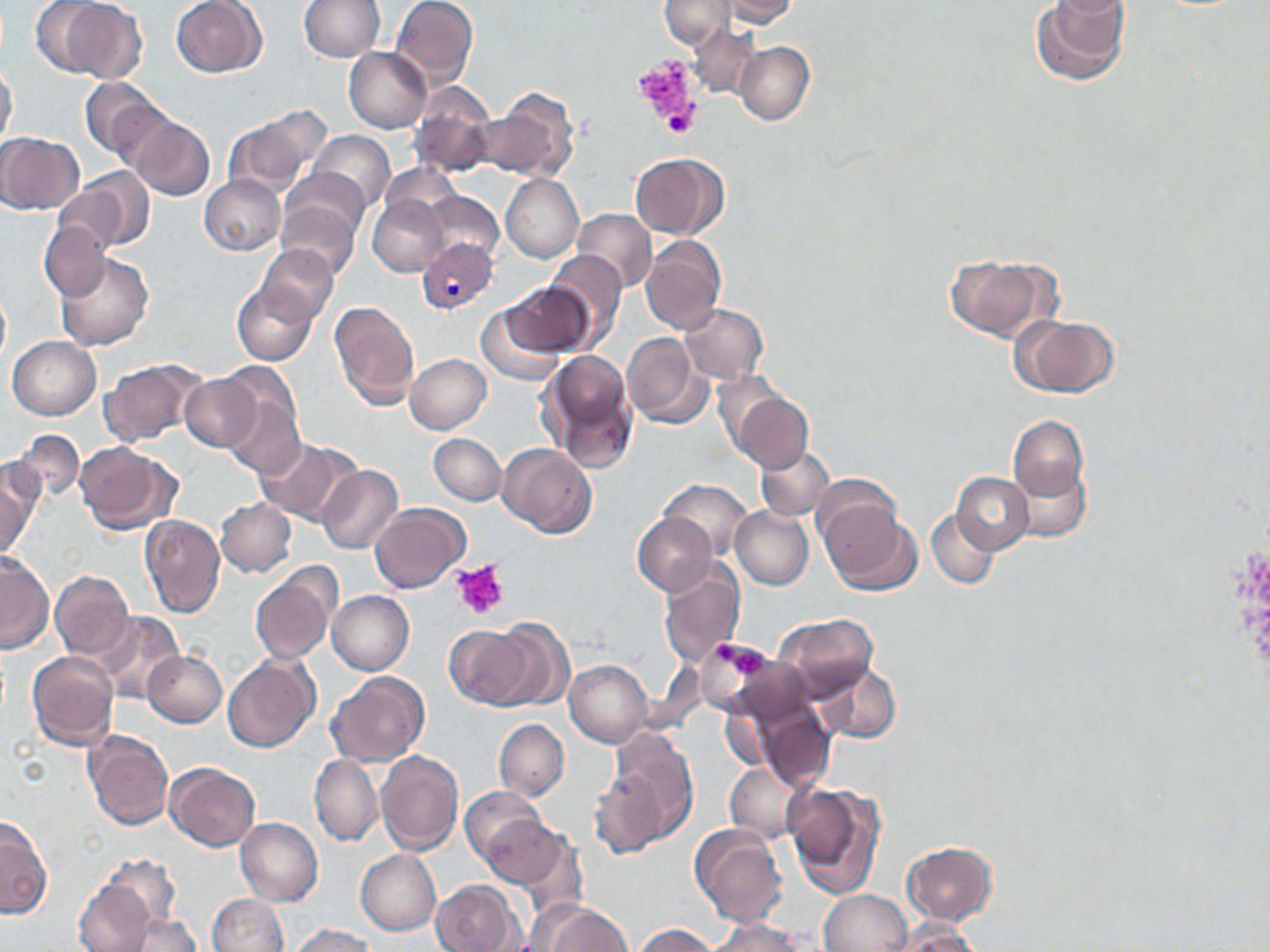

{
  "slide_level_diagnosis": "Plasmodium vivax",
  "field_of_view": "one of a larger specimen",
  "image_size": "1270×952 pixels",
  "magnification": "1000x",
  "uninfected_red_blood_cell_locations": "approximate bounding boxes as (x1, y1, x2, y2) in pixels: (31, 0, 145, 80), (171, 0, 266, 78), (299, 0, 385, 60), (392, 0, 480, 87), (661, 0, 736, 48), (713, 0, 800, 26), (1030, 0, 1132, 88), (688, 23, 760, 96), (734, 41, 814, 126), (343, 47, 432, 133), (1, 64, 17, 147), (79, 76, 163, 162), (411, 83, 500, 181), (481, 89, 579, 185), (220, 105, 331, 200), (129, 115, 214, 201), (311, 130, 395, 211), (0, 132, 83, 215), (631, 153, 728, 240), (63, 169, 154, 251), (281, 171, 371, 247), (502, 173, 584, 262), (200, 175, 285, 256), (425, 190, 504, 268), (367, 194, 448, 276), (277, 195, 362, 280), (571, 209, 656, 292), (40, 220, 107, 300), (641, 235, 726, 335), (255, 245, 339, 326), (55, 251, 154, 351), (545, 251, 628, 349), (944, 253, 1059, 342), (233, 279, 319, 367), (502, 283, 594, 358), (0, 288, 10, 366), (329, 301, 420, 412), (476, 301, 566, 387), (680, 304, 768, 383), (1013, 314, 1120, 399), (621, 333, 713, 431), (7, 336, 101, 420), (541, 349, 637, 469), (405, 354, 491, 433), (98, 356, 204, 446), (216, 363, 306, 475), (179, 374, 260, 451), (731, 390, 813, 475), (1009, 415, 1090, 501), (12, 429, 85, 505), (429, 433, 506, 505), (253, 436, 361, 527), (75, 441, 173, 532), (496, 442, 597, 538), (757, 443, 835, 522), (1012, 453, 1092, 543), (0, 457, 41, 560), (318, 465, 403, 555), (952, 470, 1034, 552), (661, 479, 752, 557), (816, 487, 919, 596), (216, 498, 297, 577), (370, 503, 470, 594), (730, 506, 813, 588), (927, 507, 999, 589), (630, 511, 716, 596), (139, 512, 226, 617), (0, 554, 51, 654), (248, 564, 340, 667), (658, 564, 746, 669), (50, 570, 133, 662), (327, 590, 416, 675), (95, 609, 185, 703), (773, 613, 878, 702), (485, 619, 573, 710), (444, 622, 536, 710), (692, 634, 782, 722), (26, 651, 119, 751), (144, 651, 227, 727), (223, 653, 320, 753), (565, 661, 654, 746), (814, 663, 900, 743), (327, 671, 429, 767), (756, 704, 834, 794), (720, 708, 773, 773), (494, 717, 568, 801), (83, 730, 175, 830), (607, 731, 699, 849), (374, 749, 464, 854), (309, 754, 381, 845), (165, 761, 261, 850), (724, 763, 799, 839), (590, 769, 666, 859), (785, 779, 887, 899), (460, 786, 548, 868), (1, 812, 51, 921), (480, 813, 569, 891), (236, 818, 324, 906), (691, 824, 790, 928), (902, 841, 997, 924), (356, 849, 440, 935), (97, 853, 181, 932), (73, 878, 159, 952), (432, 878, 522, 951), (819, 890, 910, 952), (206, 892, 290, 951), (540, 903, 634, 951), (117, 912, 204, 950), (886, 918, 982, 951), (706, 919, 807, 952), (286, 923, 378, 952), (632, 924, 717, 952)",
  "platelet_locations": "approximate bounding boxes as (x1, y1, x2, y2) in pixels: (635, 58, 693, 119), (658, 96, 698, 140), (454, 561, 507, 620), (714, 640, 735, 660), (734, 650, 765, 675)",
  "modality": "optical microscopy",
  "stain": "May-Grünwald-Giemsa",
  "plasmodium_vivax_infected_red_blood_cell_locations": "approximate bounding boxes as (x1, y1, x2, y2) in pixels: (418, 238, 497, 315)",
  "preparation": "thin blood film"
}